Describe the morphology of the red blood cells.
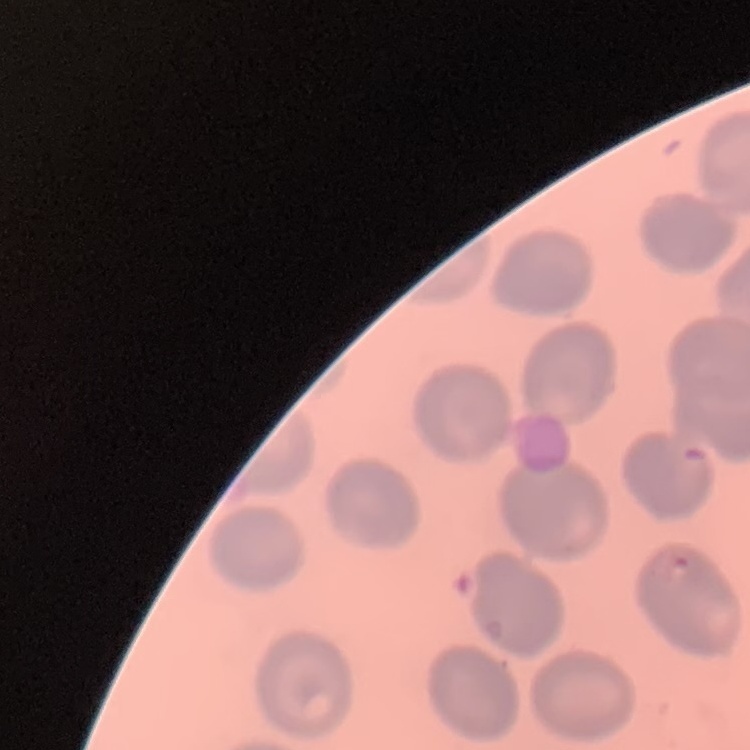
No rouleaux formation.

Summary:
  - Image type: one tile cut from a larger photomicrograph
  - Preparation: thin blood smear
  - Stain: Field's or Giemsa